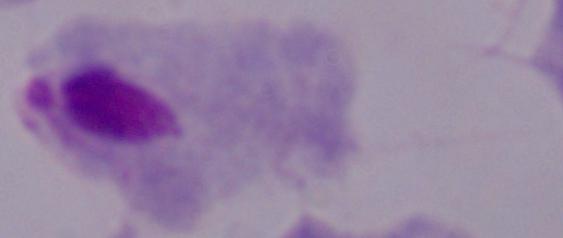

Photomicrograph. Captured at 1000x magnification. A trichomonad is seen.